Describe the morphology of the red blood cells.
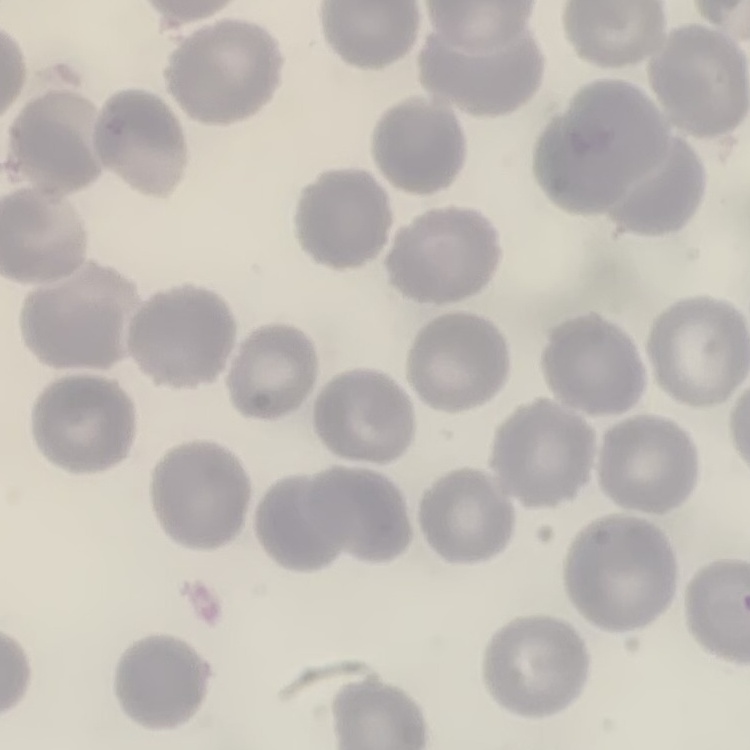

They show no rouleaux formation.

Summary:
  - Stain: Field's or Giemsa
  - Preparation: thin blood film
  - Image type: square crop of a larger photomicrograph